Locate every leukocyte (white blood cell).
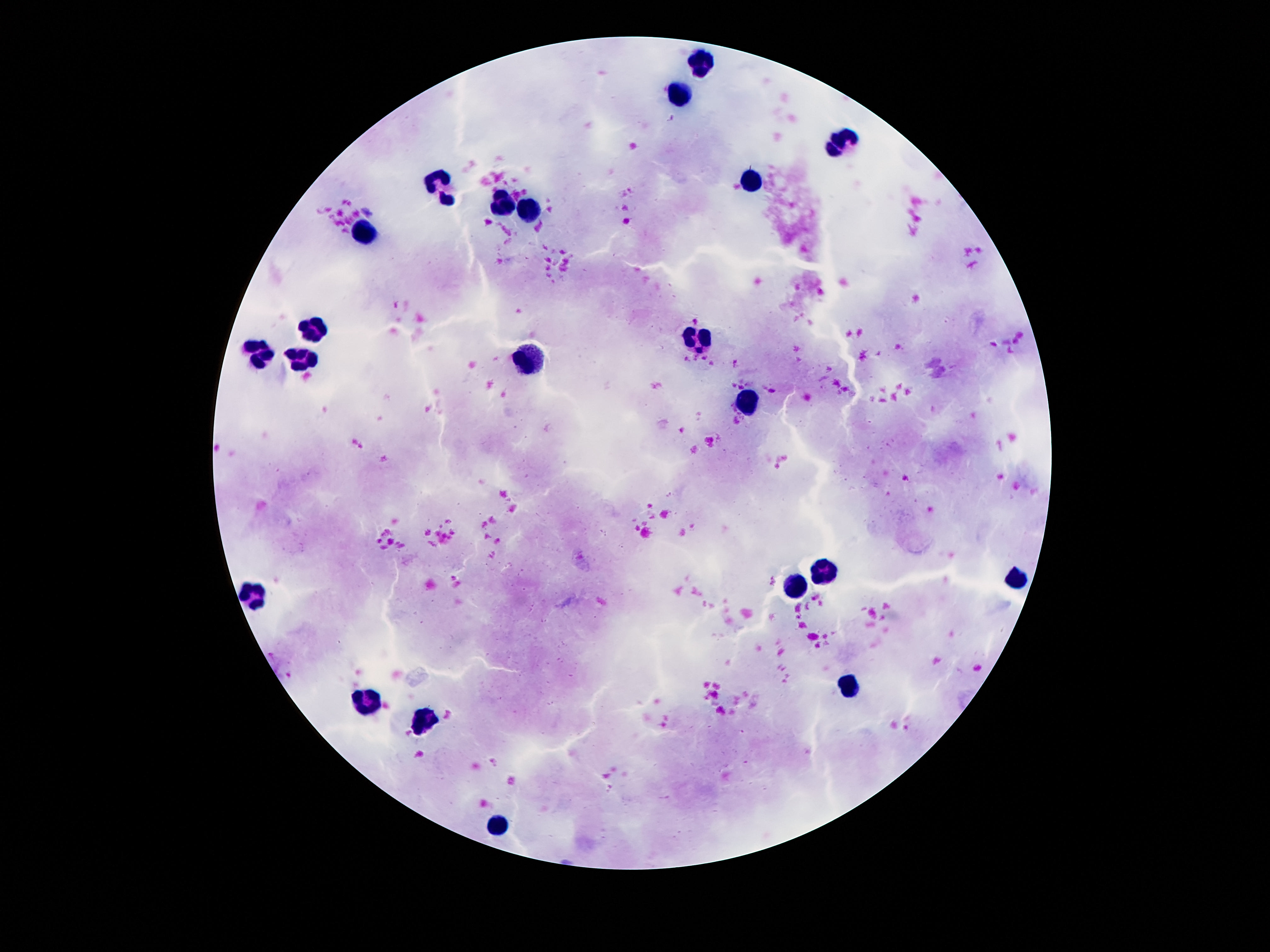
Approximate centers as {x, y} in pixels.
Leukocytes: {706, 62}, {682, 96}, {838, 145}, {754, 180}, {437, 186}, {506, 203}, {534, 212}, {364, 235}, {316, 326}, {695, 337}, {258, 353}, {532, 360}, {304, 361}, {747, 401}, {822, 569}, {1016, 580}, {795, 588}, {252, 593}, {851, 684}, {370, 700}, {420, 720}, {499, 822}.

Summary:
  - Preparation: thick peripheral-blood smear
  - Magnification: 100x
  - Field of view: single
  - Capture: smartphone camera through the microscope eyepiece
  - Stain: Giemsa
  - Image size: 1270×952 pixels
  - Patient malaria status: uninfected